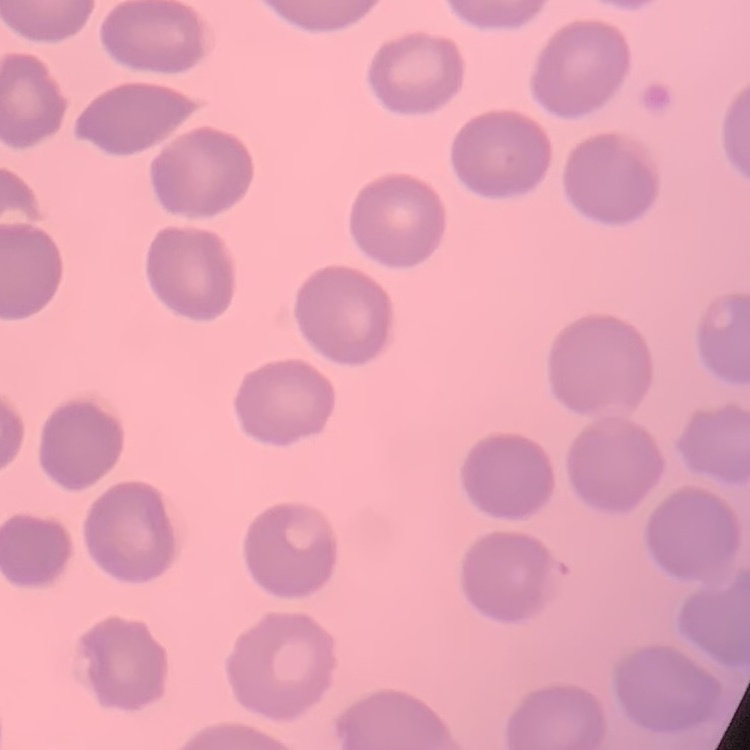 The red blood cells exhibit no rouleaux formation. Square crop of a larger photomicrograph. Field's or Giemsa stain. Thin peripheral smear.